Point out each Plasmodium parasite.
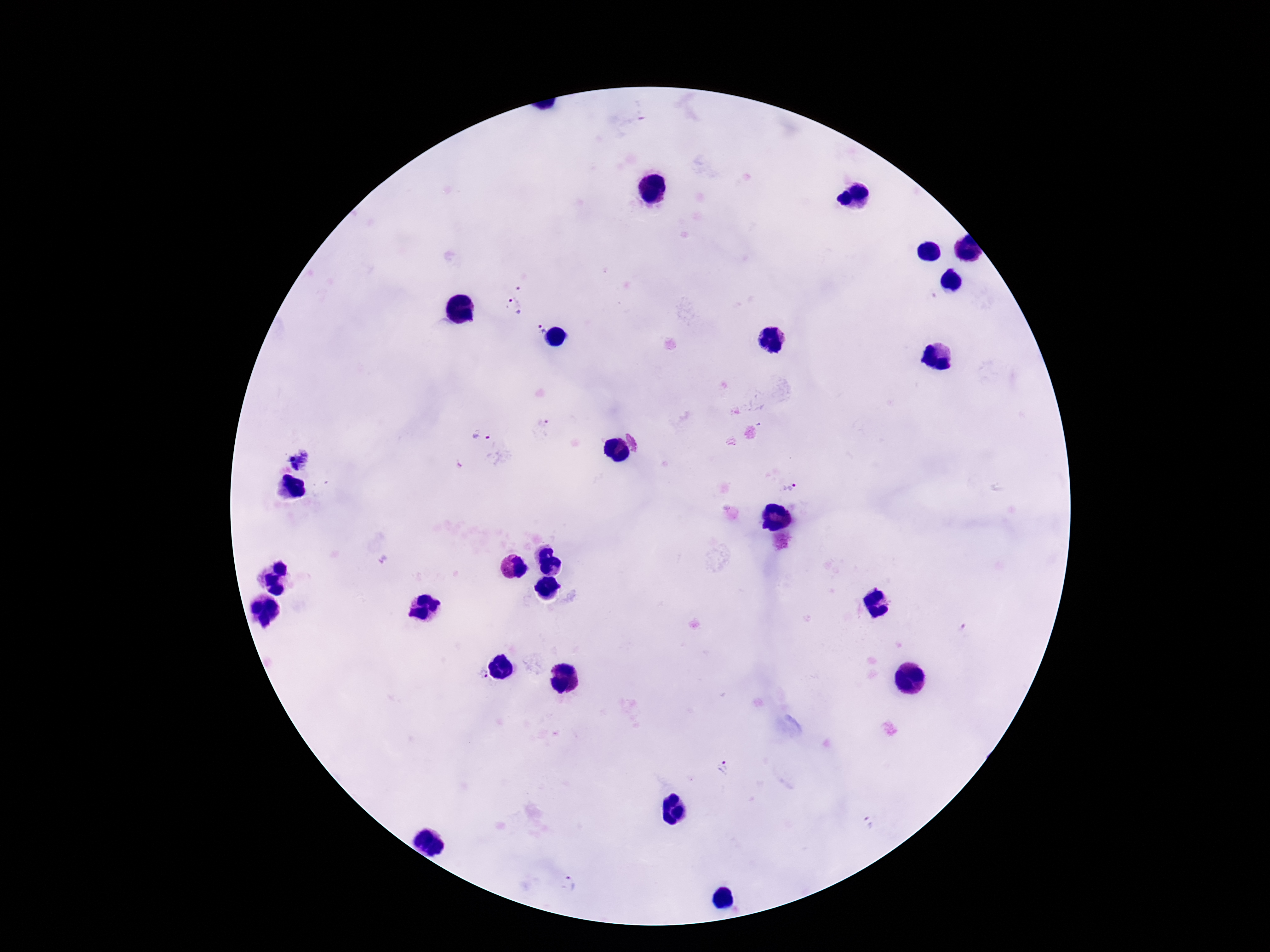
Approximate centers as {x, y} in pixels.
Plasmodium parasites: {521, 280}, {511, 308}, {540, 328}, {544, 424}, {482, 435}, {788, 487}, {385, 561}, {482, 674}, {726, 768}, {869, 822}, {568, 881}.

patient malaria status = positive
capture = smartphone camera through the microscope eyepiece
image size = 1270×952 pixels
field of view = one from this slide
stain = Giemsa
preparation = thick blood smear
magnification = 100x